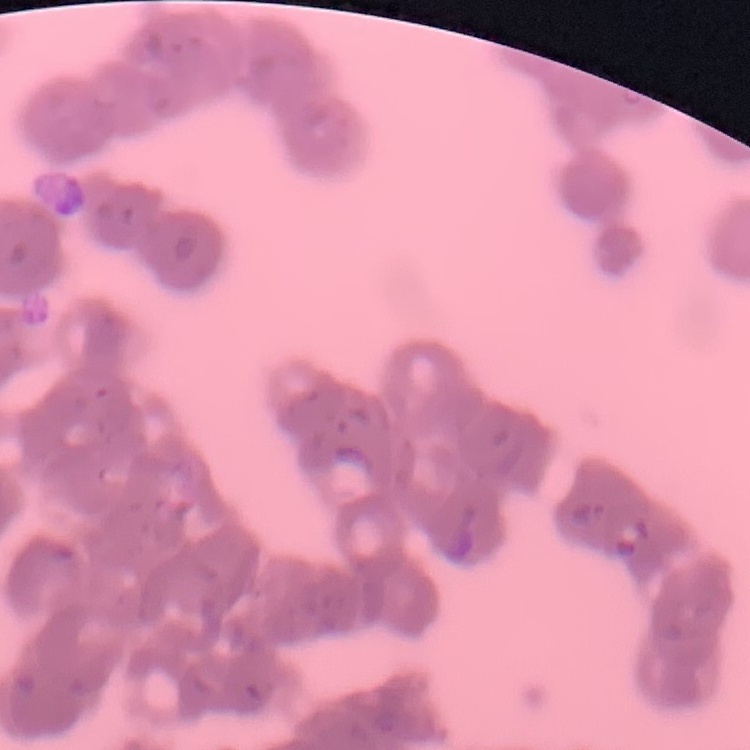 The red blood cells exhibit rouleaux formation. Stained with either Field's or Giemsa. Thin peripheral smear. One tile cut from a larger photomicrograph.